Assess for Plasmodium parasites.
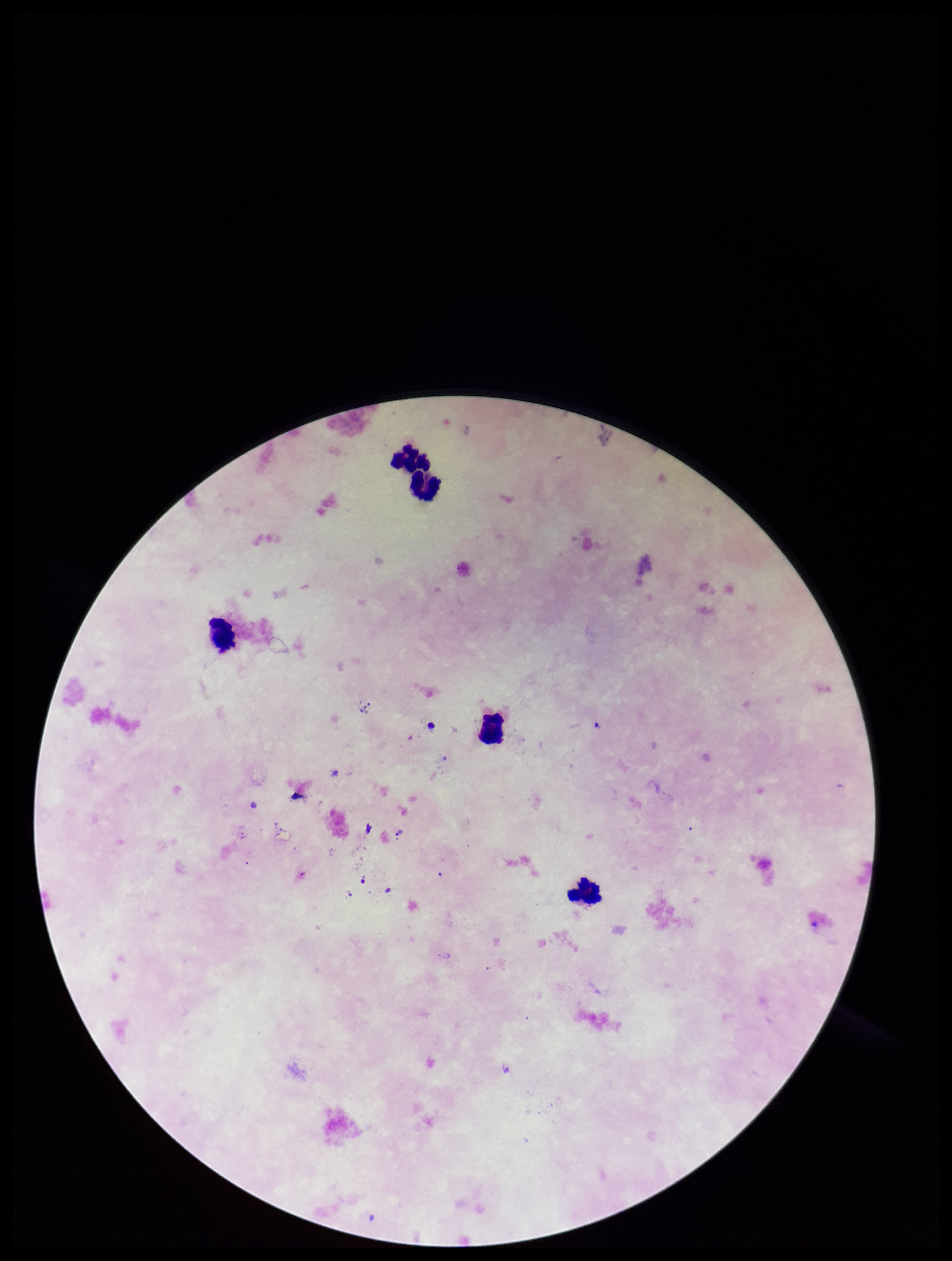
None seen.

Summary:
  - Capture: smartphone photograph through the microscope eyepiece
  - Image size: 952×1261 pixels
  - Leukocyte count: 5
  - Parasite count: 0
  - Stain: Giemsa
  - Patient malaria status: negative
  - Field of view: single
  - Preparation: thick smear